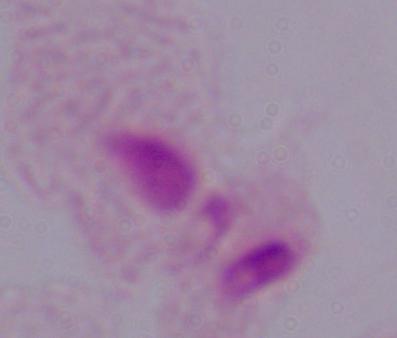 1000x magnification. A trichomonad is shown. Micrograph.